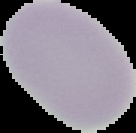 Image is 136×133 pixels. Malaria status: uninfected. From a thin blood smear. The area outside the segmented cell region is set to black.